Identify the parasite.
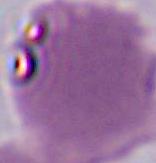

Plasmodium.

Captured at either 400x or 1000x magnification. Micrograph.